Outline each Plasmodium ovale-infected red blood cell.
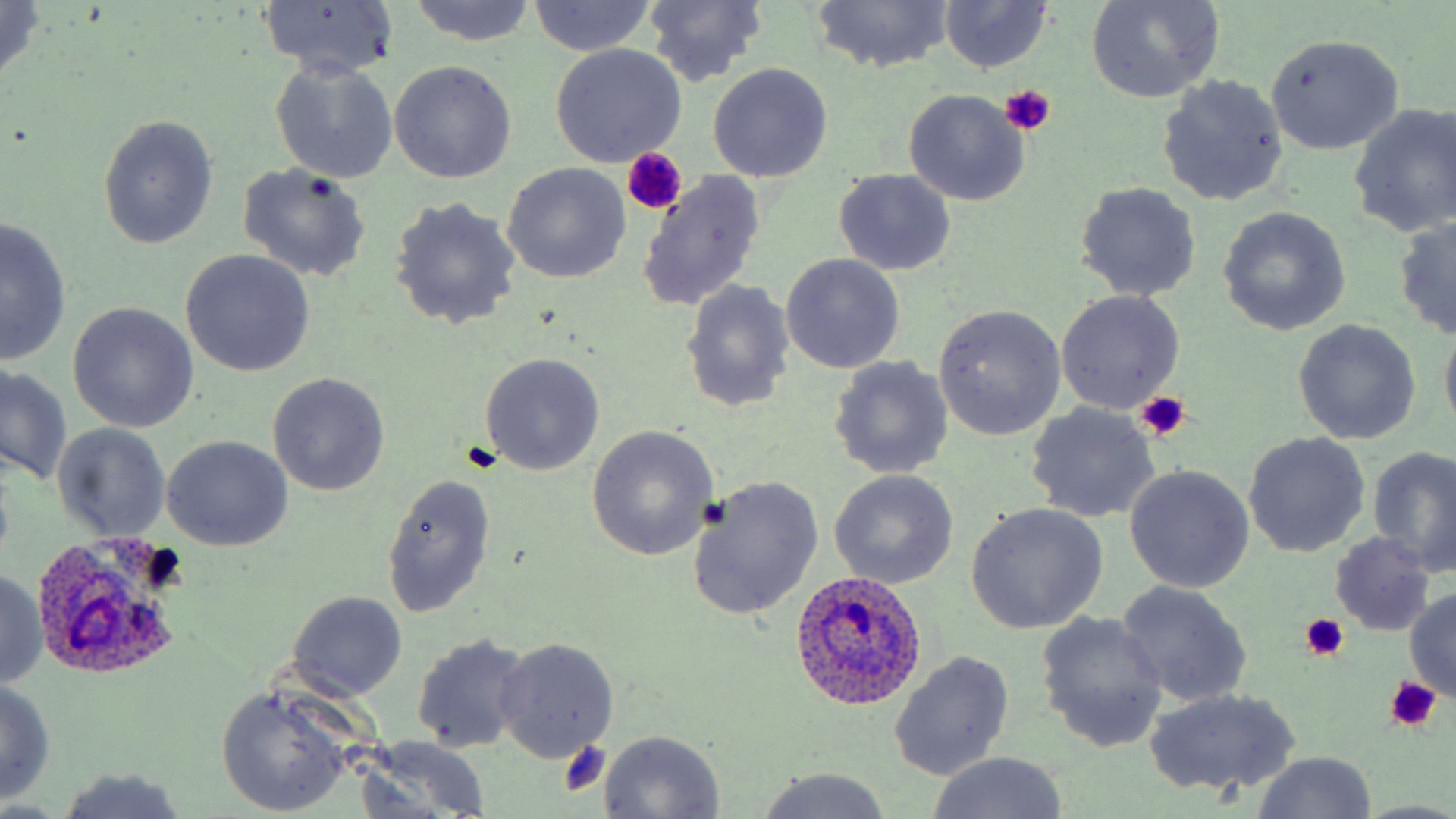
Approximate bounding boxes as named x1/y1/x2/y2 corners in pixels.
Plasmodium ovale-infected red blood cells: (x1=31, y1=532, x2=187, y2=677), (x1=788, y1=569, x2=928, y2=712).

Summary:
  - Platelet locations: (x1=1000, y1=87, x2=1055, y2=137), (x1=621, y1=150, x2=685, y2=216), (x1=1136, y1=391, x2=1192, y2=440), (x1=460, y1=441, x2=499, y2=475), (x1=1299, y1=613, x2=1349, y2=660), (x1=1384, y1=676, x2=1441, y2=730), (x1=559, y1=741, x2=610, y2=795)
  - Uninfected red blood cell locations: (x1=526, y1=0, x2=655, y2=57), (x1=939, y1=0, x2=1054, y2=74), (x1=0, y1=1, x2=47, y2=88), (x1=257, y1=1, x2=400, y2=80), (x1=408, y1=1, x2=536, y2=44), (x1=640, y1=1, x2=766, y2=86), (x1=1086, y1=1, x2=1224, y2=103), (x1=812, y1=2, x2=954, y2=72), (x1=1266, y1=33, x2=1404, y2=155), (x1=549, y1=44, x2=687, y2=166), (x1=270, y1=60, x2=398, y2=184), (x1=389, y1=61, x2=516, y2=184), (x1=707, y1=63, x2=834, y2=183), (x1=1158, y1=75, x2=1288, y2=206), (x1=902, y1=89, x2=1031, y2=205), (x1=1349, y1=102, x2=1456, y2=238), (x1=98, y1=115, x2=218, y2=249), (x1=235, y1=162, x2=370, y2=283), (x1=501, y1=163, x2=631, y2=284), (x1=833, y1=169, x2=958, y2=274), (x1=637, y1=170, x2=767, y2=311), (x1=1074, y1=182, x2=1202, y2=302), (x1=389, y1=196, x2=521, y2=330), (x1=1216, y1=207, x2=1351, y2=336), (x1=1392, y1=216, x2=1456, y2=340), (x1=1, y1=219, x2=71, y2=365), (x1=180, y1=250, x2=314, y2=377), (x1=780, y1=254, x2=906, y2=374), (x1=679, y1=280, x2=796, y2=414), (x1=1057, y1=290, x2=1185, y2=413), (x1=67, y1=302, x2=199, y2=433), (x1=933, y1=304, x2=1066, y2=440), (x1=1291, y1=319, x2=1421, y2=446), (x1=1439, y1=323, x2=1456, y2=441), (x1=478, y1=352, x2=604, y2=477), (x1=829, y1=357, x2=953, y2=478), (x1=1, y1=364, x2=73, y2=486), (x1=268, y1=372, x2=389, y2=495), (x1=1026, y1=403, x2=1159, y2=523), (x1=53, y1=423, x2=171, y2=542), (x1=586, y1=425, x2=718, y2=561), (x1=1243, y1=432, x2=1370, y2=556), (x1=162, y1=435, x2=292, y2=551), (x1=1369, y1=445, x2=1456, y2=576), (x1=1124, y1=465, x2=1254, y2=593), (x1=830, y1=471, x2=958, y2=589), (x1=380, y1=473, x2=496, y2=620), (x1=685, y1=476, x2=824, y2=620), (x1=965, y1=503, x2=1107, y2=634), (x1=1328, y1=533, x2=1436, y2=635), (x1=0, y1=569, x2=49, y2=688), (x1=1117, y1=581, x2=1253, y2=707), (x1=1403, y1=590, x2=1456, y2=701), (x1=288, y1=591, x2=407, y2=701), (x1=1035, y1=612, x2=1169, y2=752), (x1=411, y1=633, x2=532, y2=754), (x1=494, y1=638, x2=619, y2=762), (x1=888, y1=649, x2=1016, y2=781), (x1=0, y1=678, x2=57, y2=805), (x1=216, y1=684, x2=355, y2=815), (x1=1146, y1=687, x2=1300, y2=797), (x1=599, y1=730, x2=725, y2=818), (x1=361, y1=737, x2=492, y2=818), (x1=1250, y1=752, x2=1378, y2=819), (x1=925, y1=753, x2=1069, y2=819), (x1=755, y1=767, x2=894, y2=818), (x1=56, y1=768, x2=188, y2=819), (x1=1352, y1=800, x2=1456, y2=819)
  - Slide-level diagnosis: Plasmodium ovale
  - Modality: optical microscopy
  - Field of view: single
  - Image size: 1456×819 pixels
  - Magnification: 1000x
  - Stain: May-Grünwald-Giemsa
  - Preparation: thin blood film